Identify the parasite.
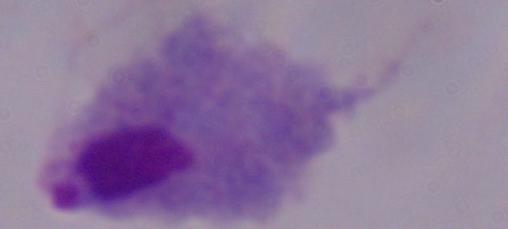

This is a trichomonad.

Summary:
  - Magnification: 1000x
  - Modality: photomicrograph